Locate every blood parasite and identify its species.
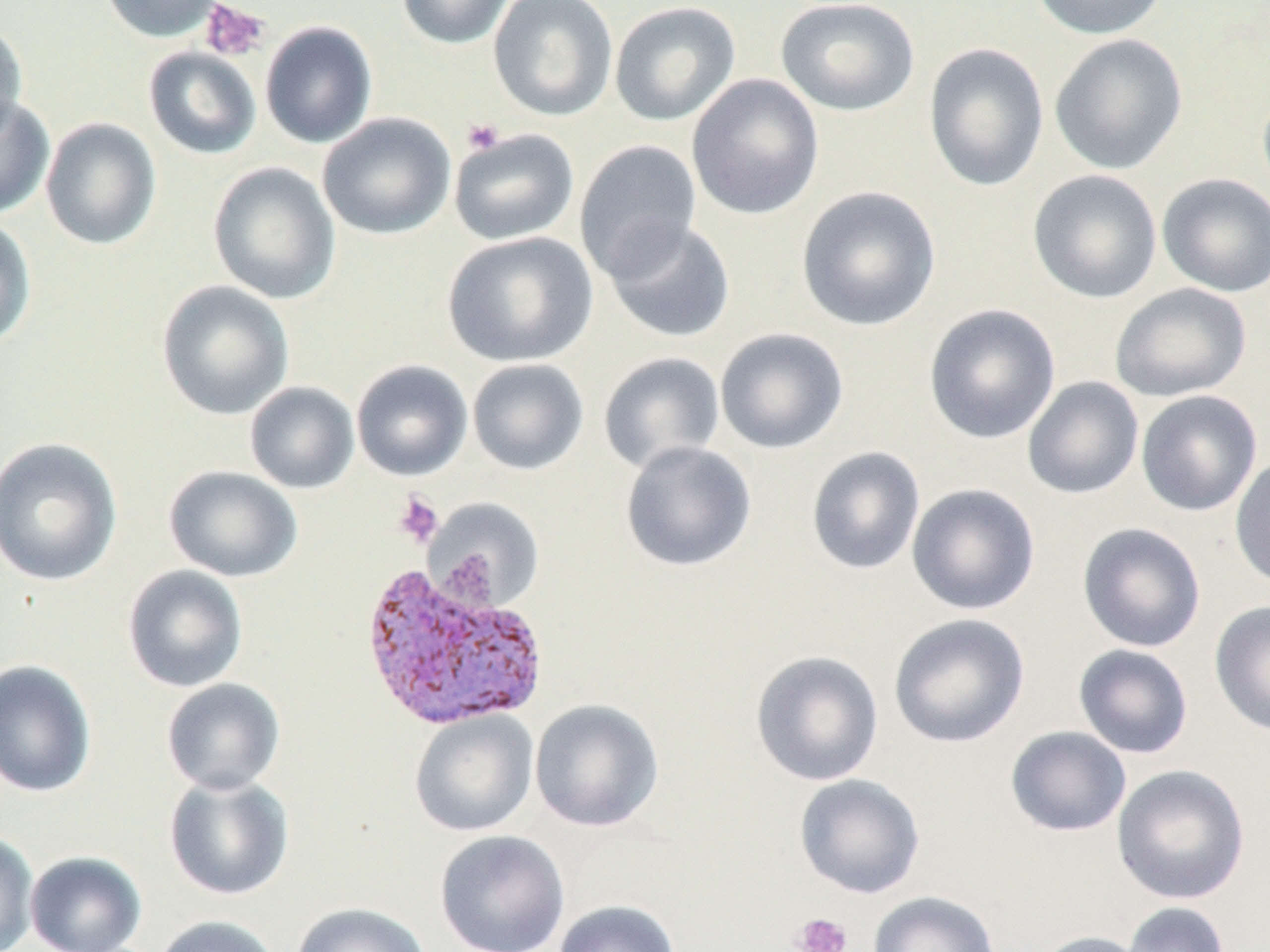
Approximate bounding boxes as (x1,y1)-(x2,y2) corner pairs in pixels.
Plasmodium vivax-infected red blood cells: (357,558)-(551,734).
No Plasmodium falciparum, Plasmodium ovale, Plasmodium malariae, Babesia divergens, or Trypanosoma brucei observed.

Platelet locations: (200,1)-(269,61), (462,118)-(505,155), (393,492)-(444,548), (790,913)-(852,952). Uninfected red blood cell locations: (100,0)-(226,43), (396,0)-(515,50), (488,0)-(618,121), (775,0)-(920,117), (1029,0)-(1169,40), (609,2)-(740,126), (0,20)-(29,140), (260,21)-(378,149), (1049,33)-(1188,175), (923,42)-(1049,192), (143,46)-(262,159), (686,73)-(824,221), (0,94)-(55,220), (317,112)-(456,240), (40,118)-(161,250), (448,128)-(579,246), (574,139)-(703,281), (207,162)-(341,305), (1027,169)-(1163,304), (1156,173)-(1270,297), (795,185)-(942,331), (0,216)-(37,349), (602,217)-(736,344), (442,231)-(597,367), (156,280)-(295,421), (1110,283)-(1251,402), (923,304)-(1061,444), (715,328)-(848,454), (597,352)-(726,475), (467,358)-(589,475), (351,359)-(473,481), (1022,376)-(1144,500), (245,381)-(360,494), (1135,390)-(1263,516), (1,436)-(123,587), (620,440)-(756,572), (806,446)-(926,575), (1229,455)-(1270,590), (163,466)-(304,583), (906,483)-(1040,615), (425,498)-(545,611), (1077,522)-(1206,652), (122,564)-(249,693), (1209,600)-(1270,737), (888,613)-(1030,748), (1073,644)-(1194,759), (750,650)-(884,786), (0,659)-(97,798), (161,678)-(286,794), (529,698)-(665,832), (409,709)-(539,837), (1005,726)-(1132,837), (1111,764)-(1250,905), (163,772)-(295,901), (793,773)-(925,899), (0,830)-(39,952), (434,830)-(570,952), (25,851)-(146,952), (868,891)-(1001,952), (552,899)-(681,952), (1121,901)-(1231,952), (291,902)-(432,952), (152,915)-(282,952), (1027,930)-(1153,952). Slide-level diagnosis: Plasmodium vivax. Thin blood film. Image is 1270×952 pixels. Single field of view. Captured at 1000x magnification. May-Grünwald-Giemsa-stained preparation. Light microscopy.